Assess the morphology of the red blood cells.
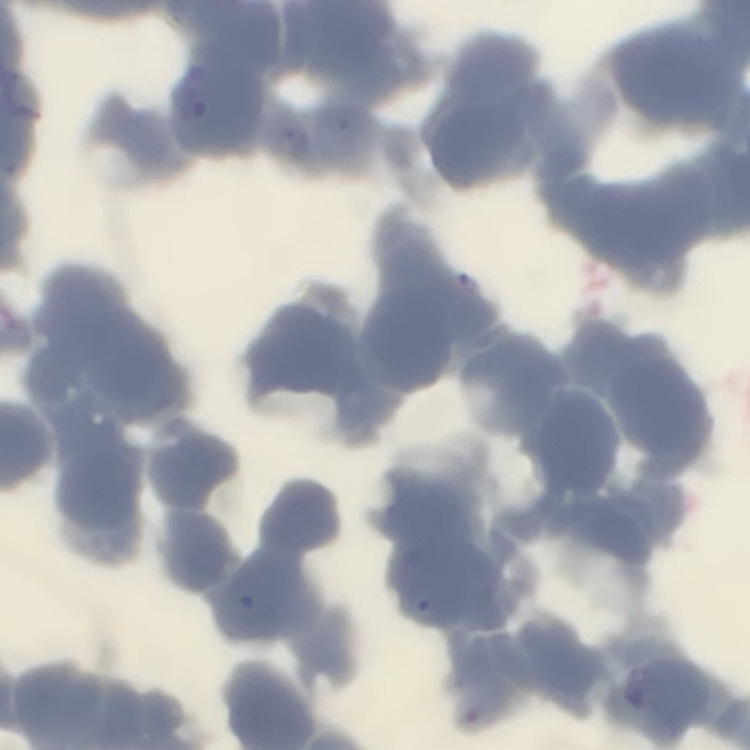
Rouleaux formation.

One tile cut from a larger photomicrograph. Thin blood film. Stained with either Field's or Giemsa.